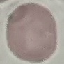

Summary:
  - Result: no malaria parasites seen
  - Image type: automatically extracted cell patch, resized to 64 × 64 pixels
  - Preparation: thin smear
  - Stain: Giemsa
  - Capture: smartphone through the microscope eyepiece